Give a bounding box for every leukocyte visible.
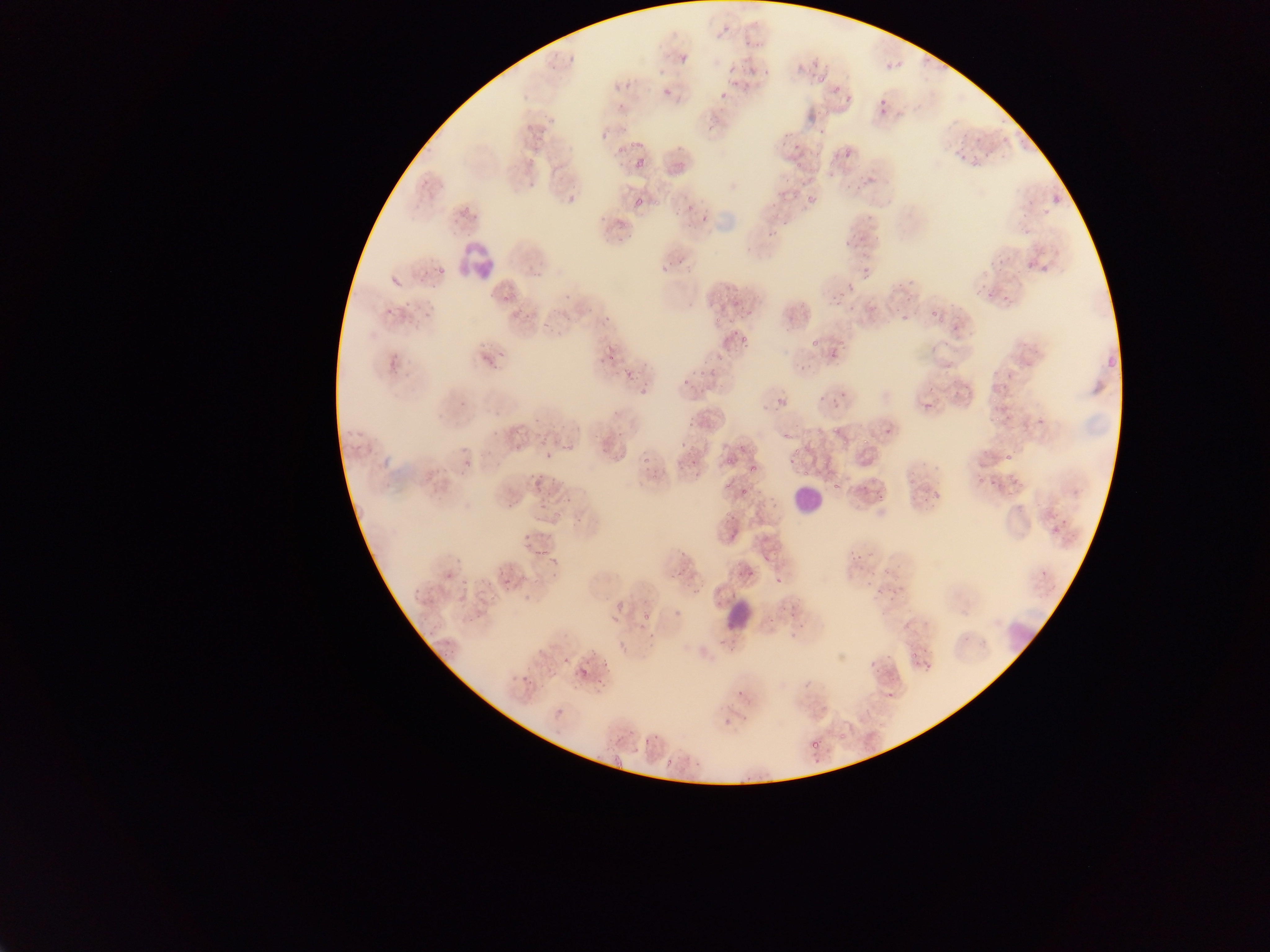
Approximate bounding boxes as (left, top, right, bottom) in pixels.
Leukocytes: (452, 235, 500, 281), (785, 477, 832, 525), (723, 604, 752, 633).

{
  "country": "Ghana",
  "capture": "mobile-phone photograph through a microscope",
  "malaria_parasite_locations": "approximate bounding boxes as (left, top, right, bottom) in pixels: (679, 56, 688, 64), (920, 59, 932, 68), (884, 61, 893, 71), (729, 66, 738, 74), (663, 86, 673, 96), (831, 87, 841, 93), (721, 92, 728, 100), (842, 100, 850, 106), (601, 132, 605, 140), (783, 133, 791, 139), (976, 134, 984, 142), (637, 142, 645, 148), (616, 144, 624, 150), (957, 144, 965, 152), (838, 146, 857, 165), (984, 148, 989, 157), (812, 152, 821, 160), (958, 154, 968, 160), (633, 157, 646, 172), (971, 159, 979, 167), (529, 183, 537, 187), (845, 184, 853, 190), (855, 184, 865, 191), (806, 192, 814, 201), (567, 196, 578, 203), (634, 197, 646, 209), (472, 211, 481, 221), (700, 214, 708, 222), (597, 215, 608, 225), (782, 218, 791, 225), (768, 227, 776, 237), (842, 237, 849, 245), (861, 267, 872, 279), (847, 279, 851, 290), (985, 285, 992, 296), (501, 290, 512, 302), (1002, 291, 1012, 302), (905, 296, 913, 302), (834, 297, 843, 305), (604, 316, 613, 322), (737, 332, 753, 350), (498, 348, 506, 358), (829, 352, 842, 360), (623, 370, 632, 375), (699, 372, 707, 376), (683, 377, 687, 385), (774, 396, 781, 404), (922, 400, 931, 412), (835, 401, 840, 409), (1035, 417, 1044, 427), (883, 425, 895, 437), (616, 432, 624, 437), (514, 444, 522, 451), (459, 447, 467, 453), (1005, 449, 1010, 462), (546, 451, 553, 461), (642, 453, 651, 461), (723, 457, 731, 465), (462, 465, 468, 475), (693, 472, 706, 480), (550, 477, 561, 481), (905, 477, 913, 486), (861, 479, 870, 488), (989, 479, 997, 487), (832, 484, 841, 490), (740, 488, 751, 493), (876, 489, 887, 502), (933, 490, 941, 498), (922, 494, 930, 503), (507, 502, 519, 508), (1052, 511, 1060, 521), (729, 515, 742, 520), (1061, 517, 1068, 525), (1049, 523, 1057, 535), (524, 534, 529, 542), (534, 551, 543, 557), (678, 551, 688, 556), (550, 554, 556, 564), (847, 556, 861, 564), (744, 568, 755, 576), (444, 574, 456, 580), (779, 576, 789, 586), (867, 579, 873, 587), (874, 590, 883, 599), (646, 613, 656, 620), (602, 659, 612, 666), (869, 660, 878, 667), (576, 667, 589, 682), (522, 672, 530, 680), (736, 691, 745, 695), (836, 733, 844, 739), (810, 735, 821, 750), (614, 757, 624, 770), (663, 759, 672, 764) | approximate (x, y) pixel centers of objects too small to bound: (725, 30), (571, 60), (766, 72), (881, 102), (881, 112), (823, 130), (966, 135), (536, 149), (796, 149), (798, 163), (830, 175), (801, 183), (794, 193), (630, 235), (620, 239), (860, 239), (680, 262), (671, 264), (934, 313), (901, 318), (718, 320), (547, 324), (612, 357), (645, 386), (844, 392), (822, 399), (785, 402), (690, 424), (517, 432), (684, 443), (564, 448), (469, 461), (791, 461), (694, 462), (752, 468), (532, 474), (540, 475), (653, 478), (730, 486), (569, 499), (541, 506), (580, 518), (859, 557), (767, 561), (1042, 572), (680, 573), (554, 575), (524, 580), (507, 582), (418, 591), (694, 592), (889, 605), (566, 660), (556, 673), (599, 682), (890, 696), (656, 737)",
  "field_of_view": "single",
  "image_size": "1270×952 pixels",
  "preparation": "thin blood smear"
}